Classify this cell by malaria status.
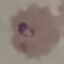
It is parasitized.

stain: Giemsa
image_type: automatically extracted cell patch, resized to 64 × 64 pixels
capture: smartphone camera at the microscope eyepiece
preparation: thin smear